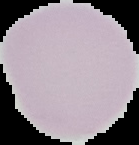

Cell region segmented out of the field of view; the surrounding area is masked to black. Image is 139×145 pixels. Result: no malaria parasites detected. From a thin blood film.